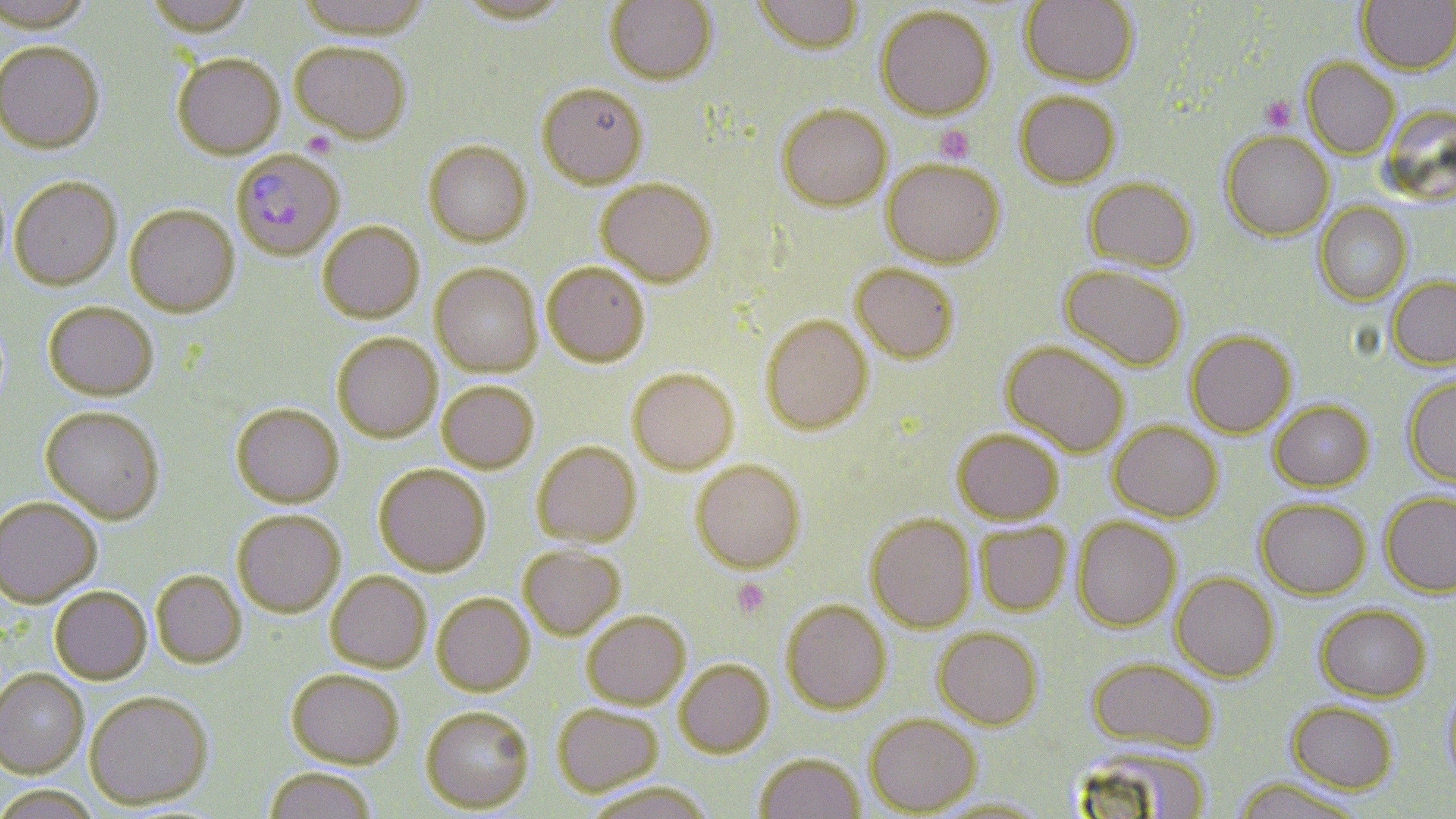
slide-level diagnosis = Plasmodium falciparum
stain = May-Grünwald-Giemsa
image size = 1456×819 pixels
uninfected red blood cell locations = approximate bounding boxes as (x1, y1, x2, y2) in pixels: (0, 0, 95, 35), (144, 0, 255, 39), (294, 0, 433, 41), (605, 0, 719, 87), (750, 0, 866, 57), (1020, 0, 1138, 88), (1356, 0, 1456, 76), (453, 1, 572, 27), (876, 6, 995, 122), (290, 42, 411, 145), (0, 43, 105, 155), (172, 54, 285, 160), (1302, 59, 1400, 160), (537, 84, 649, 189), (1014, 92, 1121, 189), (1384, 100, 1455, 211), (777, 105, 891, 211), (1221, 132, 1335, 242), (423, 141, 533, 248), (881, 159, 1006, 268), (8, 178, 121, 291), (596, 178, 717, 287), (1084, 179, 1197, 273), (1314, 203, 1412, 307), (124, 206, 239, 319), (317, 222, 424, 324), (542, 263, 649, 367), (850, 263, 959, 363), (430, 264, 543, 377), (1058, 264, 1186, 371), (1387, 277, 1456, 370), (44, 302, 158, 402), (761, 315, 873, 434), (1185, 331, 1297, 438), (333, 333, 442, 442), (1001, 341, 1129, 457), (628, 369, 739, 474), (1403, 377, 1456, 486), (437, 382, 539, 473), (1269, 400, 1374, 491), (231, 404, 345, 508), (41, 407, 165, 525), (1109, 421, 1223, 522), (952, 428, 1063, 524), (532, 442, 641, 546), (691, 459, 806, 572), (374, 464, 492, 577), (1380, 491, 1456, 597), (0, 497, 101, 607), (1255, 498, 1371, 599), (232, 510, 346, 617), (866, 513, 976, 633), (1073, 516, 1181, 631), (975, 522, 1072, 616), (518, 544, 625, 640), (151, 570, 246, 667), (326, 571, 431, 672), (1171, 571, 1280, 682), (50, 587, 152, 684), (432, 592, 535, 695), (781, 599, 892, 714), (1315, 604, 1431, 701), (582, 610, 690, 709), (933, 627, 1043, 729), (1086, 657, 1220, 753), (675, 659, 774, 757), (0, 668, 89, 777), (286, 669, 404, 767), (1440, 683, 1456, 793), (84, 690, 214, 809), (1287, 701, 1398, 793), (552, 702, 663, 797), (421, 705, 535, 812), (865, 713, 981, 815), (1073, 742, 1212, 818), (755, 752, 865, 818), (263, 767, 377, 819), (1233, 777, 1364, 819), (584, 780, 714, 819), (0, 784, 101, 819), (929, 796, 1052, 818)
platelet locations = approximate bounding boxes as (x1, y1, x2, y2) in pixels: (1258, 96, 1296, 132), (935, 125, 976, 163), (731, 577, 772, 618)
magnification = 1000x
preparation = thin blood smear
field of view = one of a larger specimen
Plasmodium falciparum-infected red blood cell locations = approximate bounding boxes as (x1, y1, x2, y2) in pixels: (231, 150, 345, 261)
modality = light microscopy